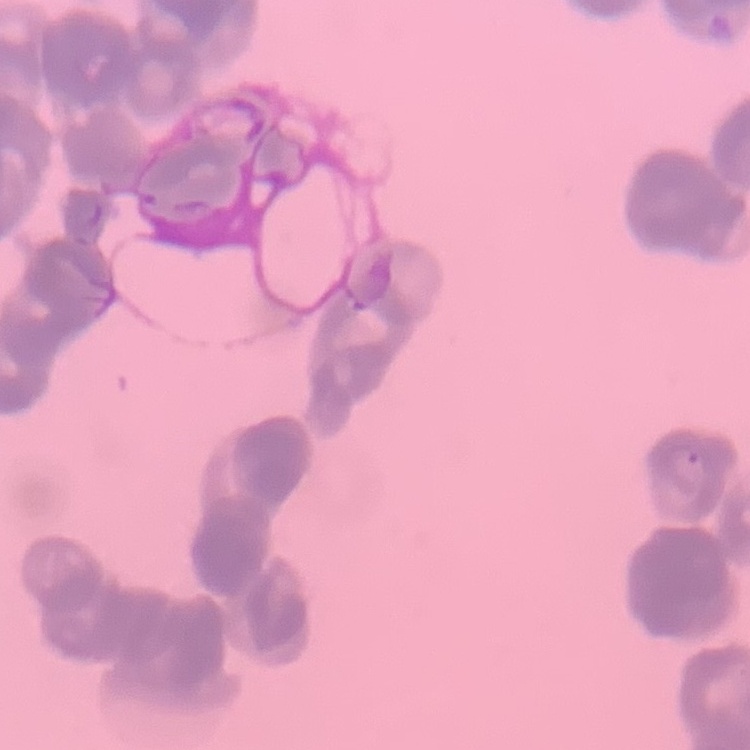 The erythrocytes exhibit rouleaux formation. Stained with either Field's or Giemsa. One tile cut from a larger photomicrograph. Thin blood film.